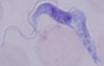

Summary:
  - Magnification: 1000x
  - Modality: photomicrograph
  - Identification: trypanosome